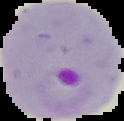

Summary:
  - Preparation: thin blood smear
  - Malaria status: parasitized
  - Image type: segmented cell region with the area outside set to black
  - Image size: 124×121 pixels